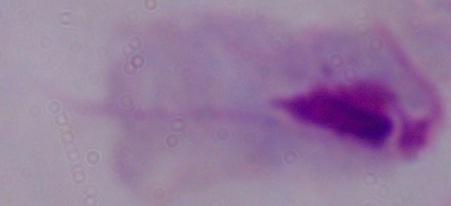
Photomicrograph. A trichomonad is shown. Captured at 1000x magnification.